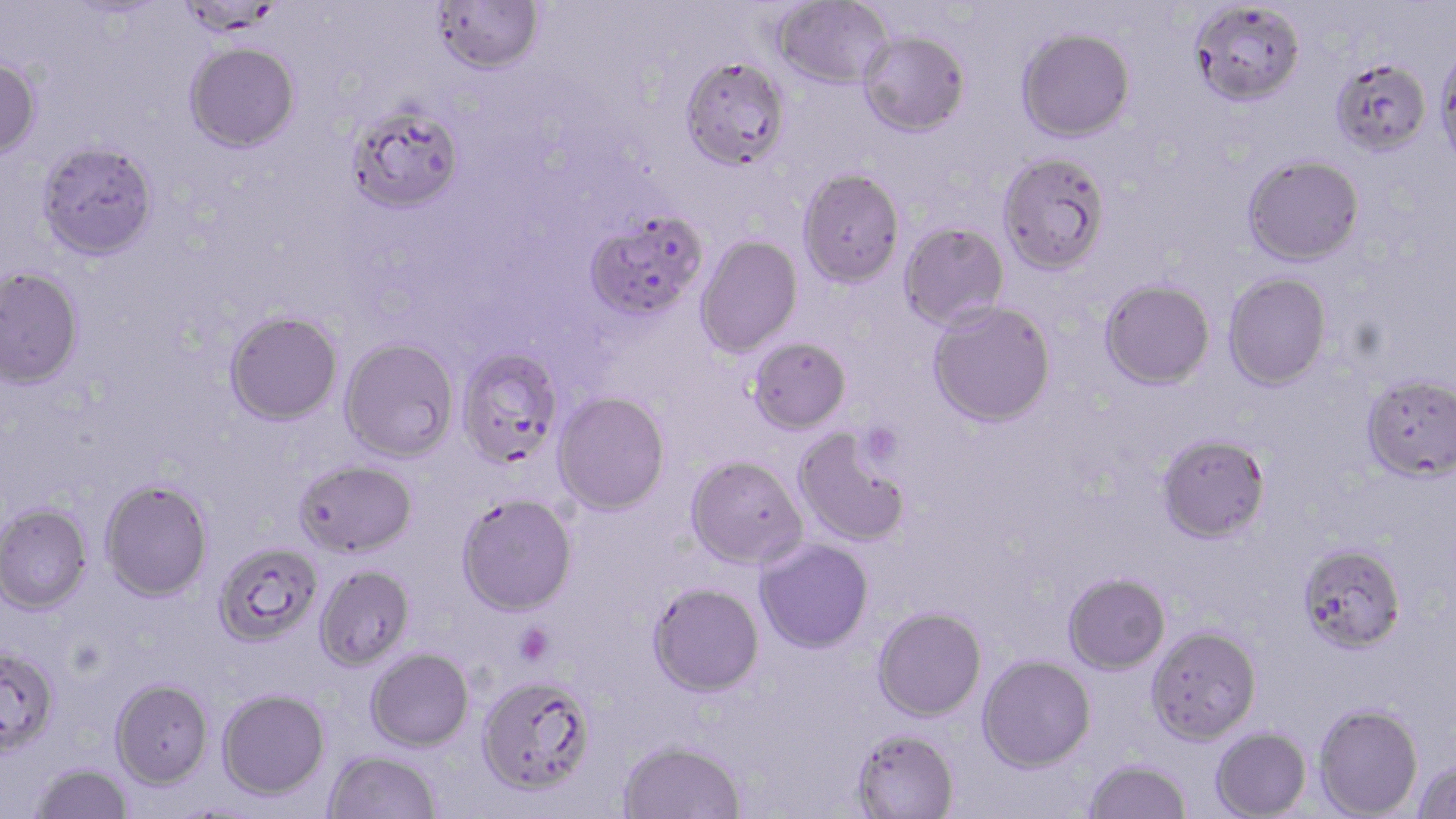

Approximate bounding boxes as (x1,y1)-(x2,y2) corner pairs in pixels. Platelet locations: (857,423)-(903,468), (514,623)-(554,666). Uninfected red blood cell locations: (432,0)-(543,74), (773,1)-(892,89), (1190,3)-(1305,106), (1016,28)-(1135,142), (858,31)-(970,136), (185,41)-(300,152), (1435,46)-(1456,169), (679,55)-(792,170), (0,56)-(43,159), (1329,56)-(1432,155), (346,101)-(465,214), (36,140)-(158,261), (997,151)-(1110,275), (1242,154)-(1365,266), (797,168)-(905,287), (583,209)-(708,322), (899,222)-(1009,330), (695,235)-(802,357), (0,265)-(84,388), (1223,273)-(1332,390), (1100,279)-(1215,389), (927,300)-(1056,427), (224,309)-(342,425), (339,337)-(459,462), (747,337)-(851,434), (456,347)-(565,468), (1360,373)-(1456,482), (553,392)-(671,515), (793,427)-(911,547), (1156,433)-(1271,543), (685,455)-(807,569), (294,459)-(418,558), (100,480)-(213,601), (456,493)-(577,616), (0,503)-(93,614), (754,539)-(873,654), (213,541)-(323,647), (1297,542)-(1407,653), (314,564)-(415,670), (1063,572)-(1170,674), (648,582)-(764,697), (872,606)-(987,721), (1146,626)-(1261,744), (0,645)-(60,756), (366,648)-(474,752), (977,655)-(1096,772), (476,674)-(596,795), (110,678)-(213,788), (217,688)-(330,799), (1314,704)-(1423,818), (852,727)-(959,819), (1210,728)-(1311,818), (618,739)-(747,819), (323,750)-(441,818), (1083,758)-(1192,819), (1413,759)-(1456,819), (30,762)-(134,818). Slide-level diagnosis: Plasmodium falciparum. Thin blood smear. 1000x magnification. May-Grünwald-Giemsa stain. Light microscopy. Image is 1456×819 pixels. One field of a larger specimen.